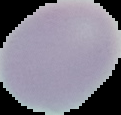

Summary:
  - Image size: 121×115 pixels
  - Image type: segmented cell region with the area outside set to black
  - Malaria status: uninfected
  - Preparation: thin blood film